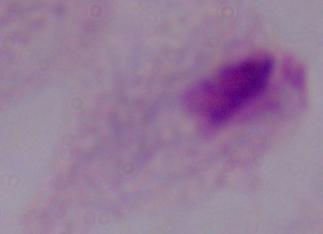

Captured at 1000x magnification. Micrograph. A trichomonad is shown.